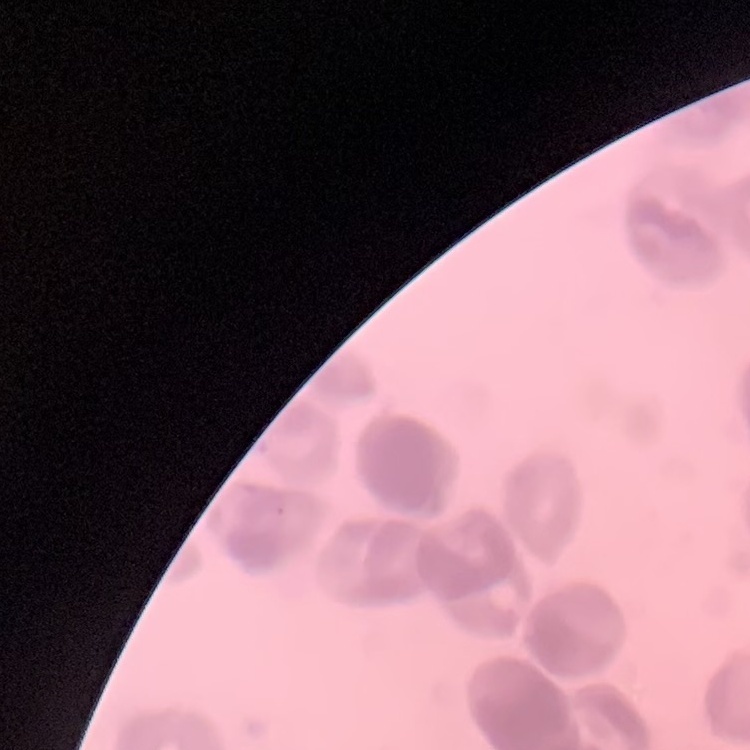
red blood cell morphology = rouleaux formation
image type = one tile cut from a larger photomicrograph
stain = Field's or Giemsa
preparation = thin blood smear